Classify this cell by malaria status.
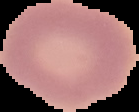

It is uninfected.

Image is 139×112 pixels. Cell region segmented out of the field of view; the surrounding area is masked to black. From a thin blood film.